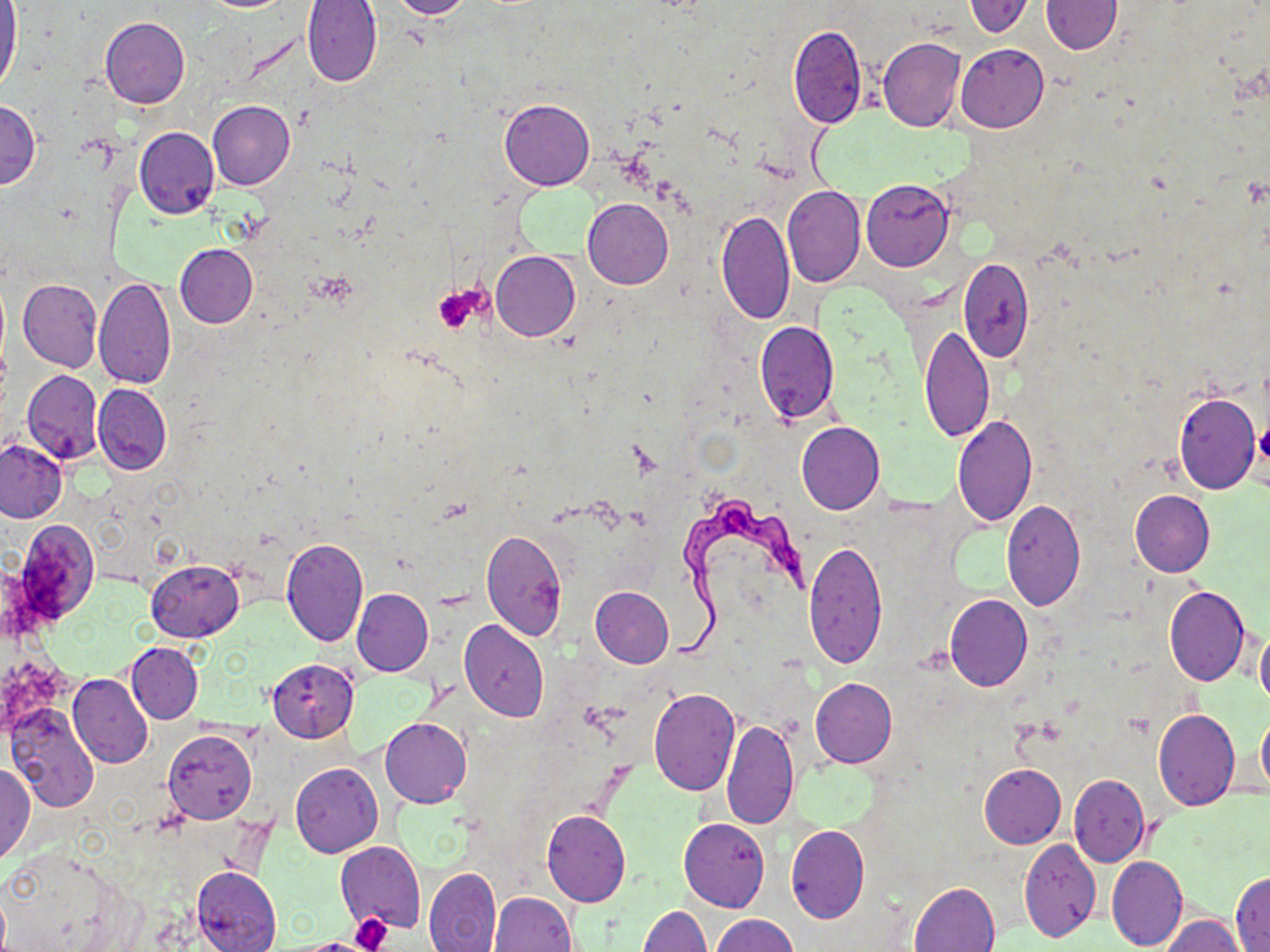
Summary:
  - Coordinate format: approximate bounding boxes as (x1,y1)-(x2,y2) corner pairs in pixels
  - Platelet locations: (432,287)-(482,332), (1257,418)-(1270,470), (350,913)-(391,952)
  - Trypanosoma brucei locations: (666,493)-(807,668)
  - Uninfected red blood cell locations: (389,0)-(475,20), (964,1)-(1032,36), (1040,1)-(1124,54), (301,2)-(383,88), (0,4)-(22,94), (100,18)-(190,108), (788,25)-(867,129), (878,36)-(966,132), (956,43)-(1049,132), (499,97)-(594,190), (0,101)-(40,189), (208,101)-(294,191), (134,127)-(219,219), (861,179)-(954,270), (782,185)-(865,287), (583,198)-(674,289), (716,210)-(796,327), (175,243)-(258,328), (491,251)-(580,341), (959,256)-(1034,360), (94,277)-(175,390), (18,279)-(101,372), (754,321)-(841,423), (920,325)-(993,443), (22,369)-(103,464), (93,383)-(171,476), (1172,391)-(1260,494), (952,414)-(1037,528), (796,421)-(885,514), (0,438)-(67,522), (1128,491)-(1214,577), (1000,500)-(1086,612), (13,519)-(100,626), (480,529)-(568,641), (279,539)-(369,646), (804,539)-(887,668), (145,559)-(243,640), (1164,584)-(1251,685), (589,587)-(673,668), (352,588)-(432,676), (945,594)-(1032,691), (459,620)-(550,721), (1255,630)-(1270,708), (127,642)-(203,723), (266,658)-(360,742), (69,673)-(153,768), (809,678)-(897,768), (648,686)-(740,795), (7,705)-(98,814), (1153,709)-(1240,811), (1257,709)-(1270,793), (380,717)-(472,809), (721,717)-(800,830), (163,729)-(255,824), (0,762)-(35,863), (290,762)-(383,858), (979,763)-(1065,848), (1069,774)-(1148,867), (541,809)-(631,907), (678,817)-(770,912), (786,825)-(869,923), (1019,838)-(1101,942), (336,841)-(426,933), (0,845)-(133,950), (1107,854)-(1187,951), (192,865)-(282,952), (424,865)-(501,952), (1231,871)-(1269,951), (910,881)-(999,952), (0,892)-(9,951), (489,892)-(578,952), (639,905)-(710,952), (711,914)-(800,952), (1163,916)-(1247,951)
  - Slide-level diagnosis: Trypanosoma brucei
  - Field of view: one of a larger specimen
  - Modality: light microscopy
  - Preparation: thin blood smear
  - Magnification: 1000x
  - Stain: May-Grünwald-Giemsa
  - Image size: 1270×952 pixels